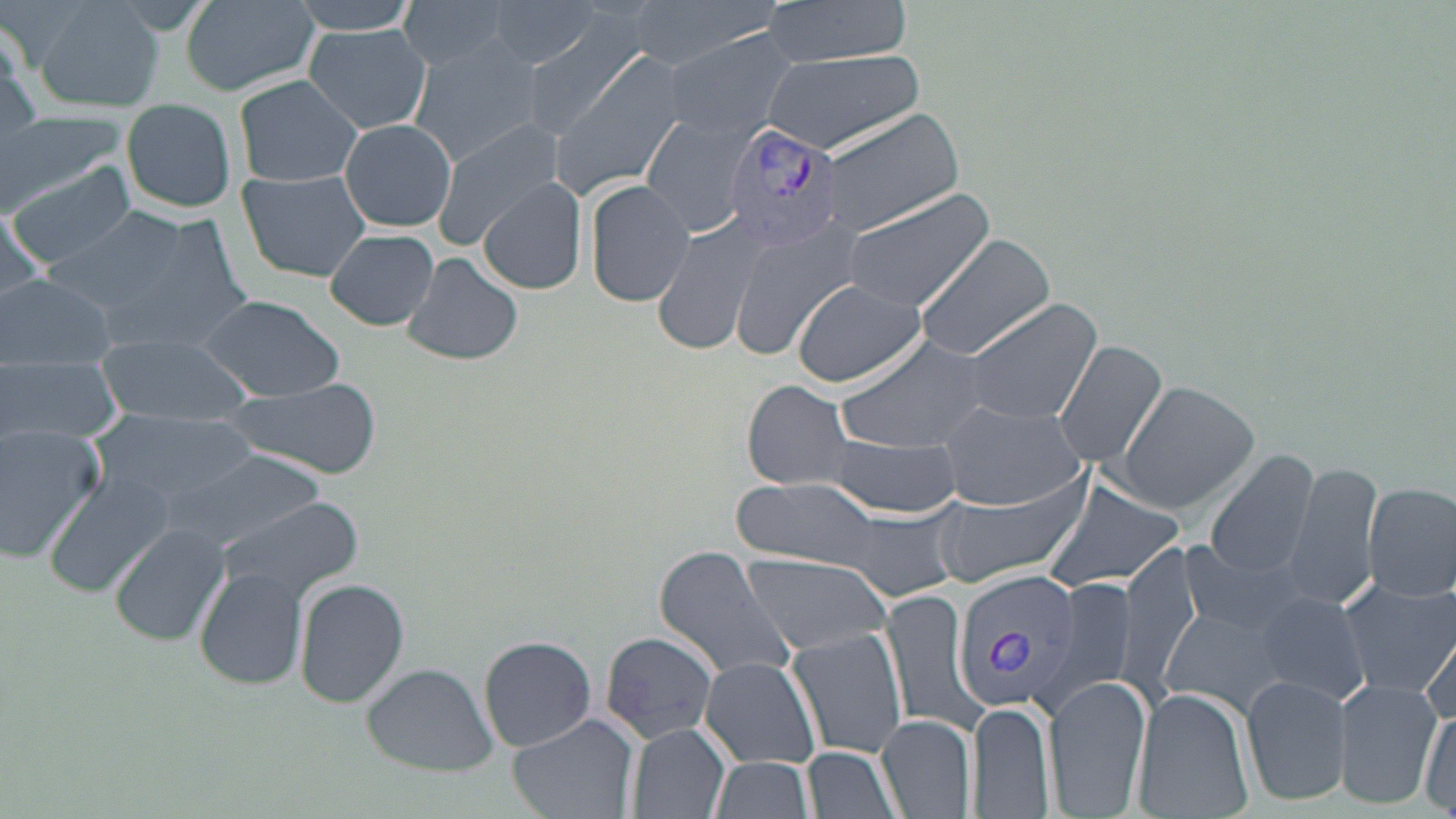
Approximate bounding boxes as (x1,y1)-(x2,y2) corner pairs in pixels. Plasmodium vivax-infected red blood cell locations: (719,121)-(843,250), (948,567)-(1084,715). Uninfected red blood cell locations: (31,0)-(165,114), (180,0)-(319,99), (288,0)-(424,37), (398,0)-(518,70), (628,0)-(778,67), (759,0)-(916,67), (484,1)-(600,68), (515,11)-(646,137), (0,18)-(38,138), (302,23)-(432,134), (662,28)-(806,142), (407,40)-(547,165), (544,41)-(690,199), (763,49)-(925,155), (234,74)-(366,190), (120,98)-(240,212), (823,108)-(963,233), (0,113)-(127,208), (642,113)-(762,237), (340,117)-(457,233), (433,120)-(565,247), (9,158)-(139,269), (236,169)-(373,282), (478,177)-(588,296), (585,178)-(695,308), (843,186)-(994,315), (46,208)-(192,308), (74,210)-(259,356), (651,210)-(774,357), (2,211)-(50,307), (730,218)-(857,362), (326,228)-(439,330), (915,235)-(1056,362), (402,252)-(522,366), (0,274)-(117,371), (792,278)-(928,385), (196,293)-(346,400), (961,298)-(1101,426), (835,334)-(995,454), (96,335)-(253,424), (1054,339)-(1168,468), (2,355)-(122,448), (743,380)-(855,490), (1113,380)-(1260,514), (222,382)-(385,477), (934,400)-(1089,510), (92,411)-(262,509), (1,425)-(106,562), (821,433)-(963,516), (169,448)-(327,555), (1204,452)-(1320,579), (1278,462)-(1382,614), (42,472)-(173,598), (731,477)-(886,568), (926,477)-(1091,590), (1040,478)-(1186,595), (1362,481)-(1456,603), (215,493)-(365,605), (834,507)-(963,602), (112,523)-(232,648), (1178,539)-(1317,641), (1119,540)-(1200,703), (654,544)-(801,686), (742,556)-(893,652), (196,567)-(307,689), (1036,574)-(1138,721), (295,577)-(409,708), (1335,578)-(1456,697), (1253,589)-(1373,707), (882,590)-(983,736), (1161,605)-(1290,712), (1422,614)-(1456,734), (787,628)-(910,758), (601,631)-(719,743), (479,635)-(595,752), (699,657)-(821,769), (362,664)-(498,776), (1241,676)-(1352,806), (1043,677)-(1153,819), (1335,678)-(1442,807), (1133,686)-(1254,819), (968,701)-(1055,818), (1418,703)-(1455,815), (508,714)-(639,819), (876,714)-(975,817), (627,721)-(732,819), (803,746)-(904,819), (707,755)-(816,819). Slide-level diagnosis: Plasmodium vivax. Single field of view. Optical microscopy. May-Grünwald-Giemsa stain. Captured at 1000x magnification. Thin blood smear. Image is 1456×819 pixels.